Locate and identify every blood parasite.
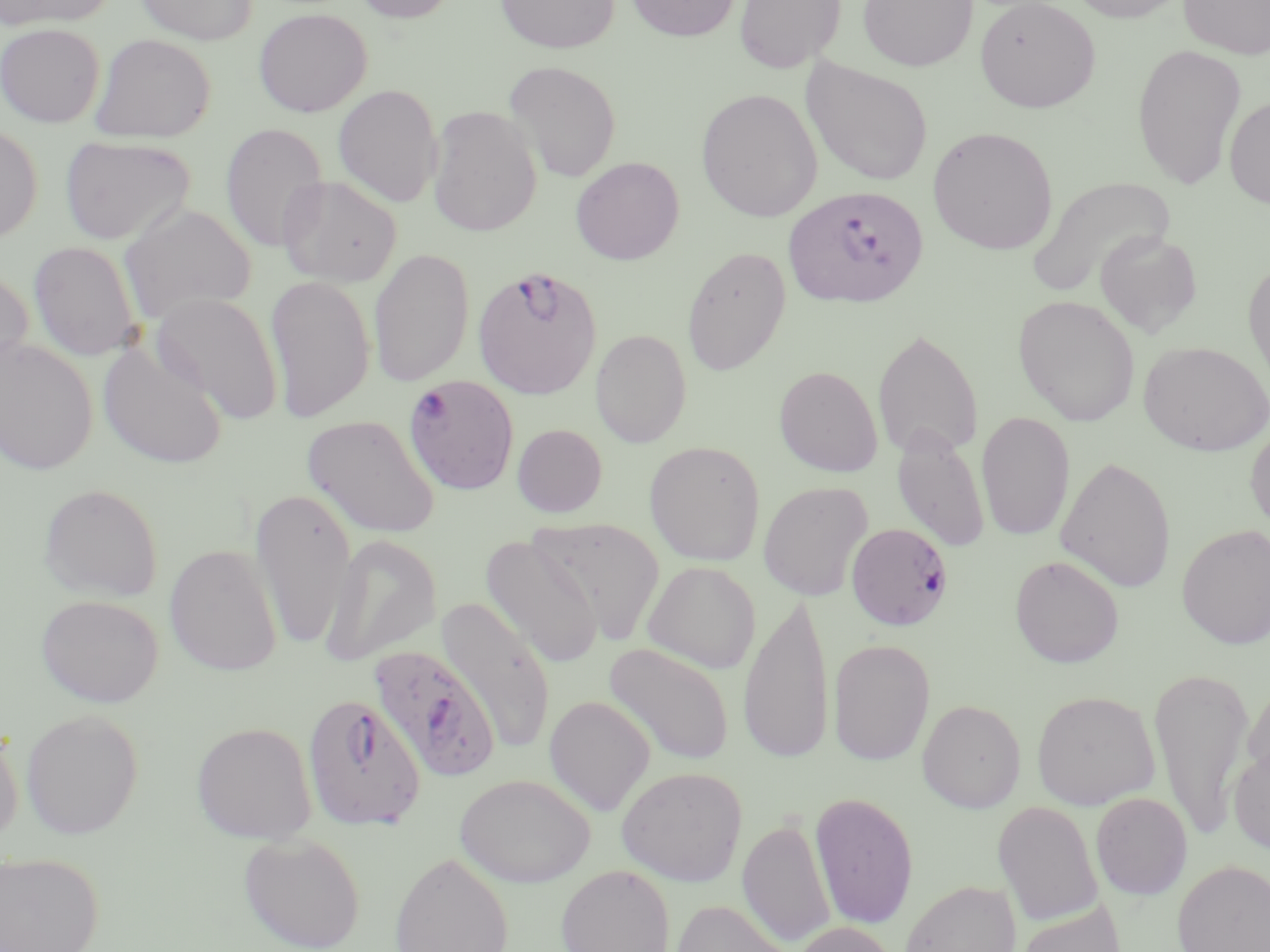

Approximate bounding boxes as (x1, y1, x2, y2) in pixels.
Plasmodium falciparum-infected red blood cells (subset): (783, 185, 930, 309), (472, 265, 603, 401), (404, 375, 519, 497), (367, 644, 500, 783), (301, 694, 427, 830).
No Plasmodium ovale, Plasmodium malariae, Plasmodium vivax, Babesia divergens, or Trypanosoma brucei observed.

{
  "slide_level_diagnosis": "Plasmodium falciparum",
  "field_of_view": "one of a larger specimen",
  "uninfected_red_blood_cell_locations_subset": "approximate bounding boxes as (x1, y1, x2, y2) in pixels: (0, 0, 116, 30), (134, 0, 258, 45), (350, 0, 460, 24), (495, 0, 619, 54), (625, 0, 740, 42), (735, 0, 845, 73), (857, 0, 978, 71), (975, 0, 1101, 113), (1064, 0, 1192, 23), (1179, 0, 1270, 60), (254, 7, 372, 117), (0, 22, 105, 128), (90, 33, 216, 143), (1132, 43, 1247, 190), (801, 59, 934, 187), (502, 60, 622, 183), (333, 84, 443, 208), (696, 88, 822, 222), (1223, 95, 1270, 209), (427, 105, 542, 237), (0, 123, 43, 244), (220, 123, 329, 253), (927, 126, 1058, 255), (60, 135, 196, 247), (571, 156, 685, 265), (277, 175, 403, 287), (1026, 176, 1176, 299), (119, 202, 257, 325), (1094, 230, 1204, 338), (28, 240, 142, 362), (682, 245, 791, 377), (368, 248, 475, 388), (1243, 257, 1270, 395), (0, 269, 34, 383), (265, 274, 375, 423), (151, 293, 283, 422), (1013, 295, 1140, 426), (872, 327, 983, 463), (590, 329, 692, 448), (0, 338, 99, 475), (97, 340, 228, 470), (1138, 340, 1269, 456), (774, 365, 883, 477), (976, 412, 1075, 542), (301, 414, 442, 539), (1245, 420, 1270, 535), (512, 423, 607, 517), (891, 425, 991, 553), (644, 441, 766, 565), (1055, 456, 1176, 593), (758, 481, 873, 601), (38, 482, 164, 602), (249, 487, 357, 649), (530, 519, 665, 644), (1177, 524, 1270, 649), (321, 534, 442, 666), (480, 535, 605, 667), (164, 543, 283, 676), (1009, 554, 1125, 668), (643, 560, 760, 674), (738, 592, 835, 766), (35, 593, 164, 707), (437, 597, 557, 755), (828, 638, 935, 765), (603, 642, 735, 766), (1148, 665, 1254, 843), (1241, 679, 1270, 791), (1031, 690, 1159, 810), (544, 695, 656, 815), (917, 699, 1026, 813), (20, 708, 144, 839), (0, 720, 23, 850), (191, 721, 318, 843), (1228, 741, 1270, 856), (616, 766, 748, 886), (454, 773, 596, 887), (810, 791, 919, 930), (1091, 792, 1193, 900), (992, 801, 1103, 926), (738, 817, 836, 948), (238, 832, 366, 952), (0, 851, 103, 952), (389, 851, 514, 952), (1173, 860, 1270, 952), (556, 864, 675, 952), (899, 880, 1022, 952), (670, 899, 800, 952), (1014, 900, 1126, 952), (791, 921, 898, 952)",
  "preparation": "thin blood film",
  "magnification": "1000x",
  "stain": "May-Grünwald-Giemsa",
  "modality": "light microscopy",
  "image_size": "1270×952 pixels"
}